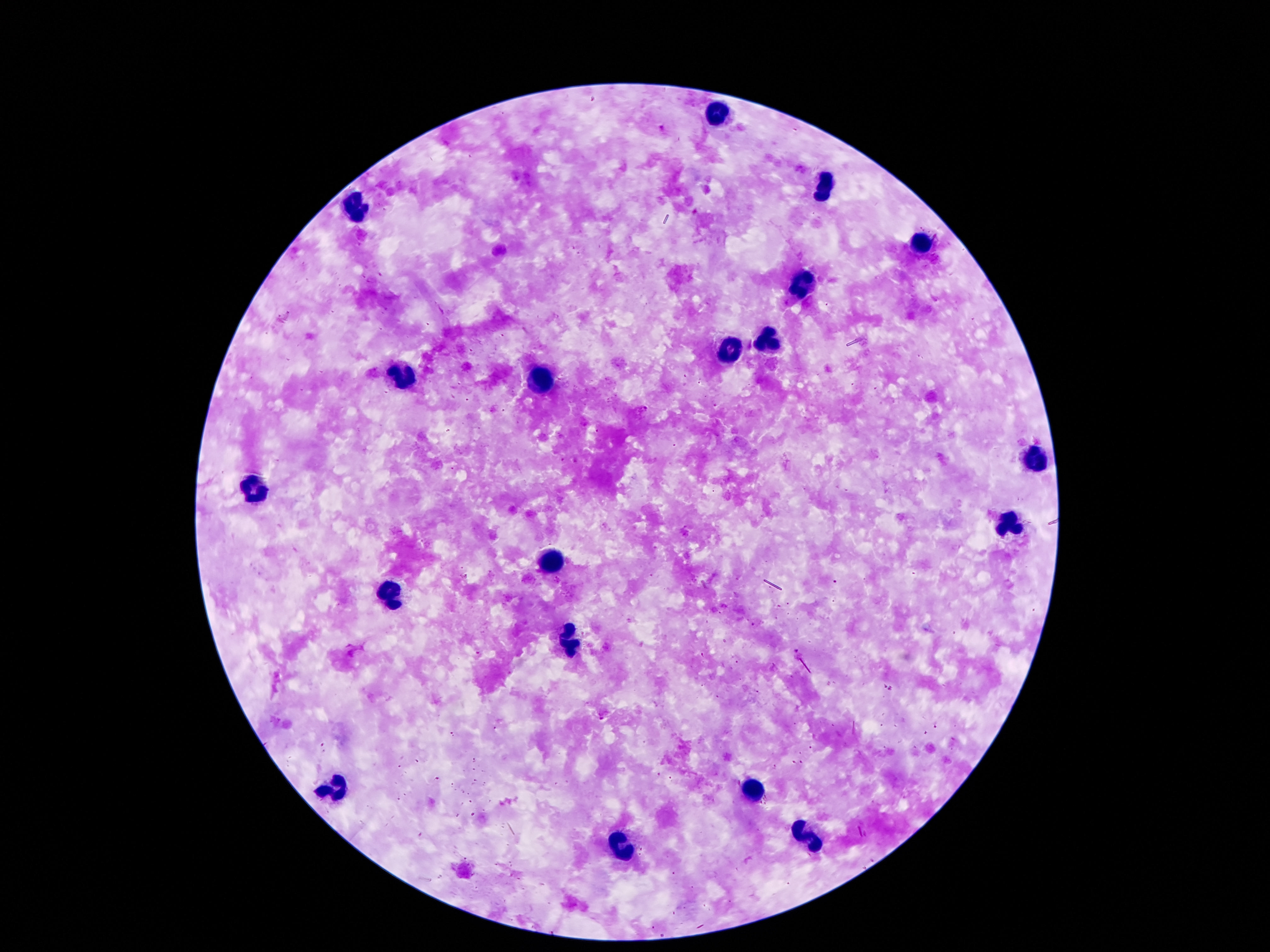

preparation = thick blood film
patient malaria status = negative
leukocyte locations = approximate object centers, in pixels from the top-left corner: (x=721, y=112), (x=824, y=188), (x=358, y=206), (x=919, y=244), (x=803, y=286), (x=768, y=343), (x=728, y=356), (x=402, y=374), (x=539, y=379), (x=1030, y=458), (x=255, y=490), (x=1007, y=530), (x=549, y=568), (x=385, y=599), (x=574, y=640), (x=339, y=786), (x=755, y=793), (x=812, y=837), (x=623, y=848)
capture = smartphone camera through the microscope eyepiece
magnification = 100x
image size = 1270×952 pixels
stain = Giemsa
field of view = single